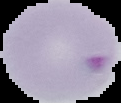
Cell region segmented out of the field of view; the surrounding area is masked to black. From a thin blood film. Image is 121×103 pixels. Malaria status: parasitized.